Assess the morphology of the erythrocytes.
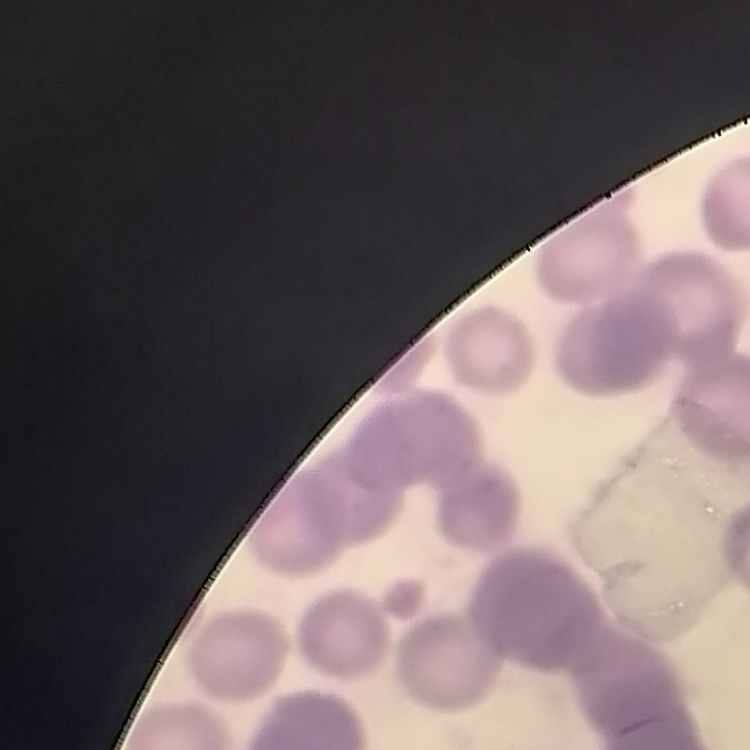

They show rouleaux formation.

One tile cut from a larger photomicrograph. Thin blood smear. Field's or Giemsa stain.